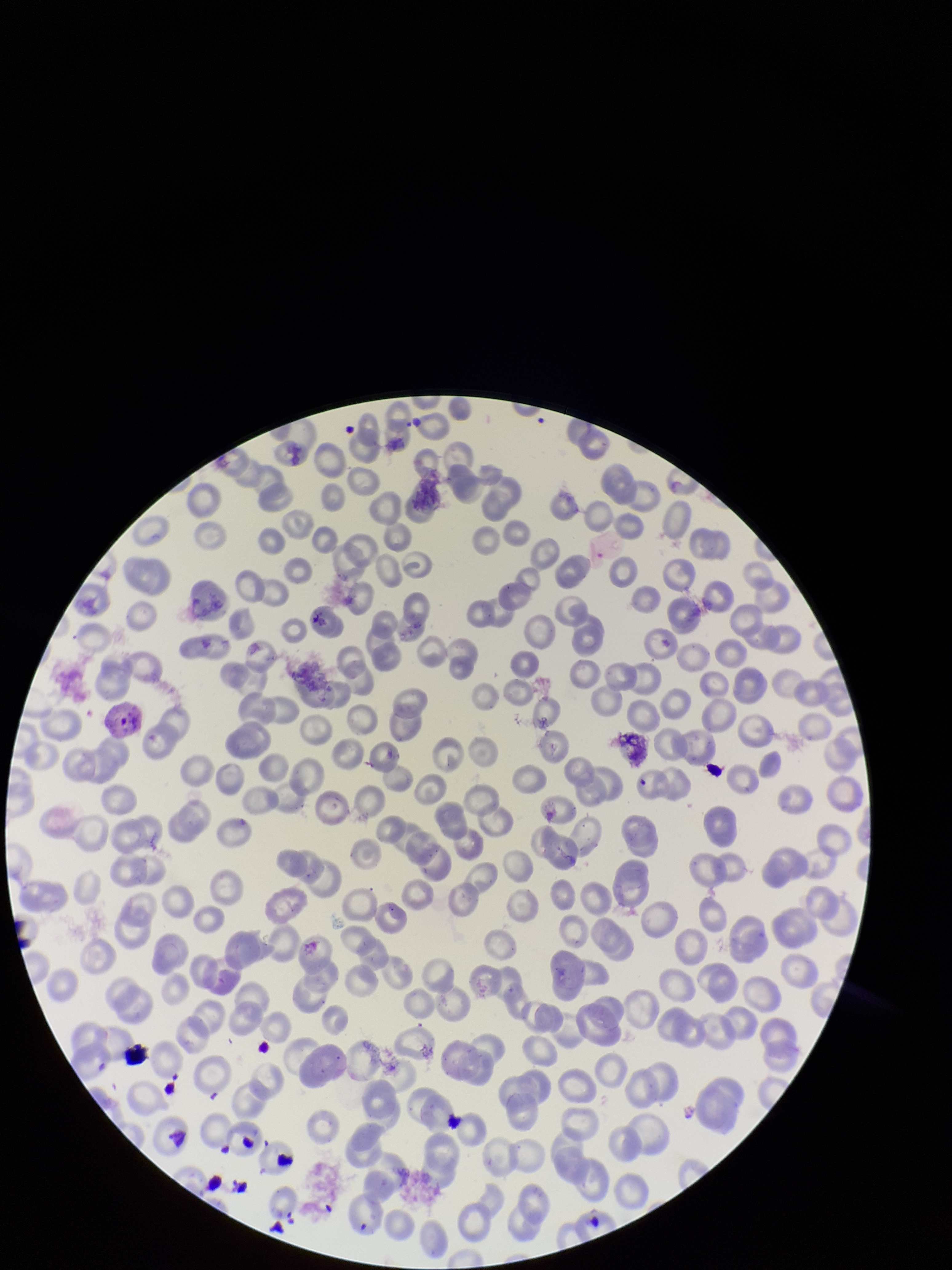
Giemsa stain. Red blood cell count: 206. Species reported for this patient: Plasmodium vivax. Preparation: thin. Parasitized red blood cell count: 1. Smartphone photograph taken through the eyepiece of a microscope. Parasitized red blood cells: identified. Patient malaria status: positive. Image is 952×1270 pixels. One field from this slide.